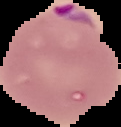

{
  "image_size": "121×127 pixels",
  "image_type": "segmented cell region on a black background",
  "preparation": "thin blood film",
  "result": "malaria parasites detected"
}